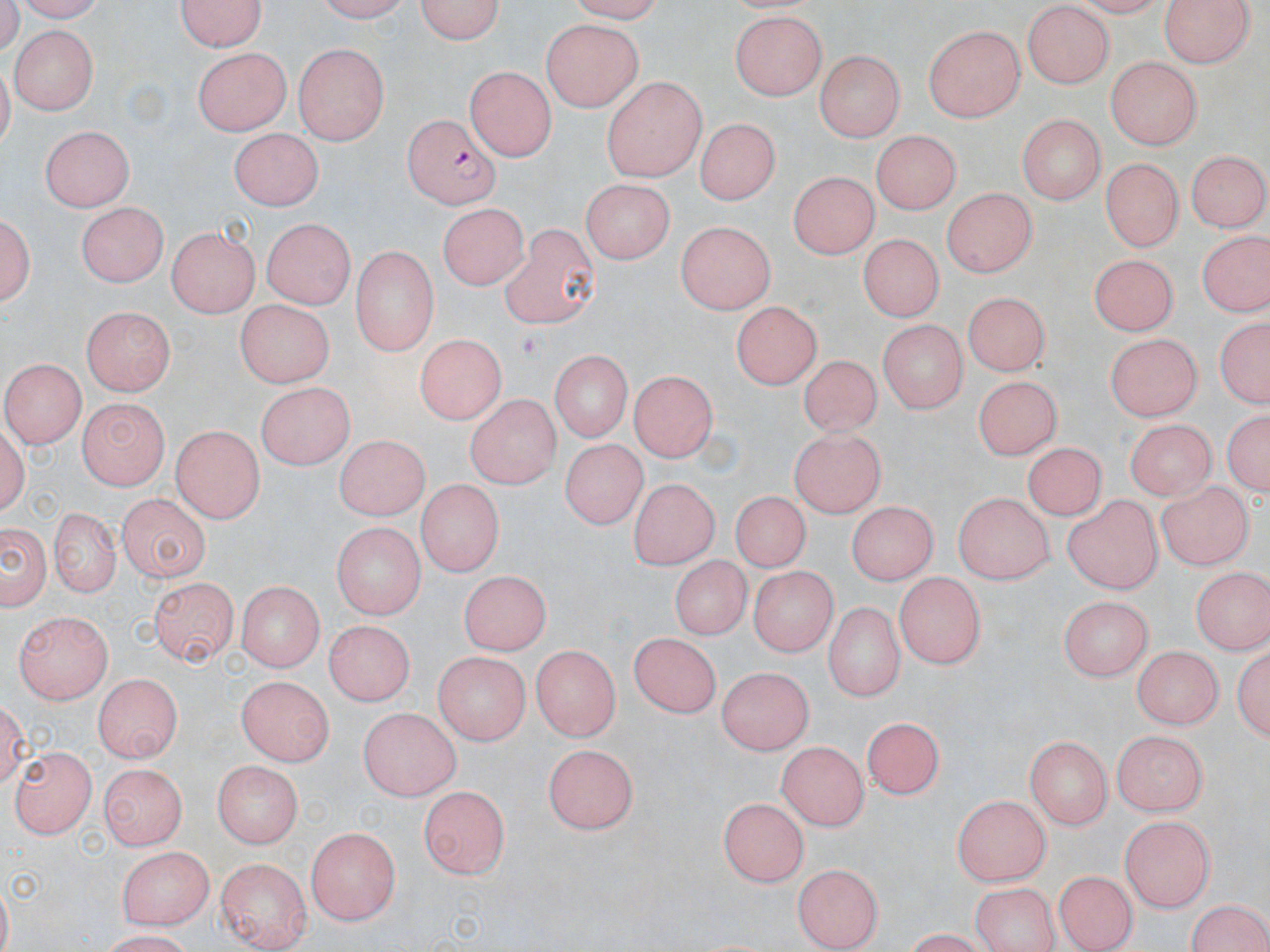 Approximate bounding boxes as [x1, y1, x2, y2] in pixels. Uninfected red blood cell locations: [176, 0, 269, 53], [414, 0, 508, 44], [1157, 0, 1256, 66], [1021, 6, 1117, 86], [729, 10, 829, 100], [543, 20, 644, 112], [923, 22, 1024, 121], [9, 26, 95, 112], [293, 42, 390, 144], [195, 47, 290, 134], [815, 49, 905, 142], [1106, 56, 1198, 150], [464, 67, 557, 161], [601, 76, 709, 182], [1015, 114, 1104, 207], [693, 122, 777, 207], [42, 124, 133, 211], [871, 128, 961, 217], [231, 129, 319, 209], [55, 130, 154, 276], [1184, 149, 1269, 233], [1102, 153, 1184, 245], [788, 169, 874, 261], [579, 177, 677, 260], [941, 187, 1034, 280], [76, 199, 170, 286], [440, 199, 533, 290], [3, 205, 36, 314], [262, 216, 353, 310], [675, 220, 774, 316], [499, 223, 602, 327], [164, 225, 262, 314], [857, 232, 941, 323], [1197, 232, 1265, 317], [351, 246, 439, 356], [1088, 250, 1178, 331], [959, 293, 1055, 374], [237, 298, 333, 387], [731, 302, 820, 391], [83, 309, 174, 396], [1212, 314, 1268, 412], [876, 320, 970, 413], [1102, 331, 1203, 420], [412, 337, 506, 425], [547, 351, 634, 443], [800, 355, 885, 437], [2, 360, 82, 448], [976, 377, 1061, 459], [626, 378, 713, 461], [255, 383, 355, 467], [467, 393, 558, 488], [79, 398, 171, 489], [1222, 406, 1268, 502], [1122, 417, 1220, 500], [171, 423, 267, 523], [788, 429, 887, 520], [331, 438, 429, 525], [564, 438, 648, 531], [1020, 446, 1114, 517], [626, 478, 721, 569], [1157, 480, 1250, 571], [414, 482, 504, 581], [118, 490, 210, 583], [733, 491, 813, 572], [949, 492, 1054, 584], [1062, 497, 1161, 592], [847, 499, 933, 588], [48, 508, 120, 596], [0, 517, 51, 617], [329, 520, 427, 618], [673, 554, 750, 642], [1190, 567, 1268, 653], [459, 569, 548, 658], [748, 569, 839, 658], [894, 573, 987, 668], [148, 578, 237, 666], [236, 579, 323, 672], [1056, 597, 1155, 681], [821, 600, 907, 701], [13, 612, 115, 707], [325, 620, 411, 707], [632, 632, 719, 720], [1235, 639, 1269, 745], [532, 643, 619, 742], [1130, 644, 1224, 729], [432, 651, 532, 742], [716, 663, 812, 757], [94, 674, 185, 764], [238, 675, 336, 761], [359, 706, 464, 797], [868, 713, 945, 794], [1109, 732, 1208, 818], [1024, 737, 1111, 829], [777, 738, 869, 830], [544, 741, 642, 832], [10, 747, 99, 837], [211, 761, 302, 848], [102, 765, 187, 852], [420, 784, 510, 879], [950, 792, 1055, 886], [717, 794, 810, 882], [1120, 816, 1215, 913], [307, 825, 400, 926], [118, 845, 213, 930], [217, 857, 311, 951], [791, 862, 881, 949], [1055, 871, 1136, 950], [967, 883, 1066, 952], [1183, 897, 1270, 952]. Plasmodium falciparum-infected red blood cell locations: [405, 113, 505, 204]. Slide-level diagnosis: Plasmodium falciparum. Image is 1270×952 pixels. Captured at 1000x magnification. One field of a larger specimen. May-Grünwald-Giemsa-stained preparation. Optical microscopy. Thin blood film.